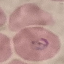
{
  "malaria_status": "parasitized",
  "preparation": "thin smear",
  "capture": "smartphone camera at the microscope eyepiece",
  "image_type": "automatically extracted cell patch, resized to 64 × 64 pixels",
  "stain": "Giemsa"
}